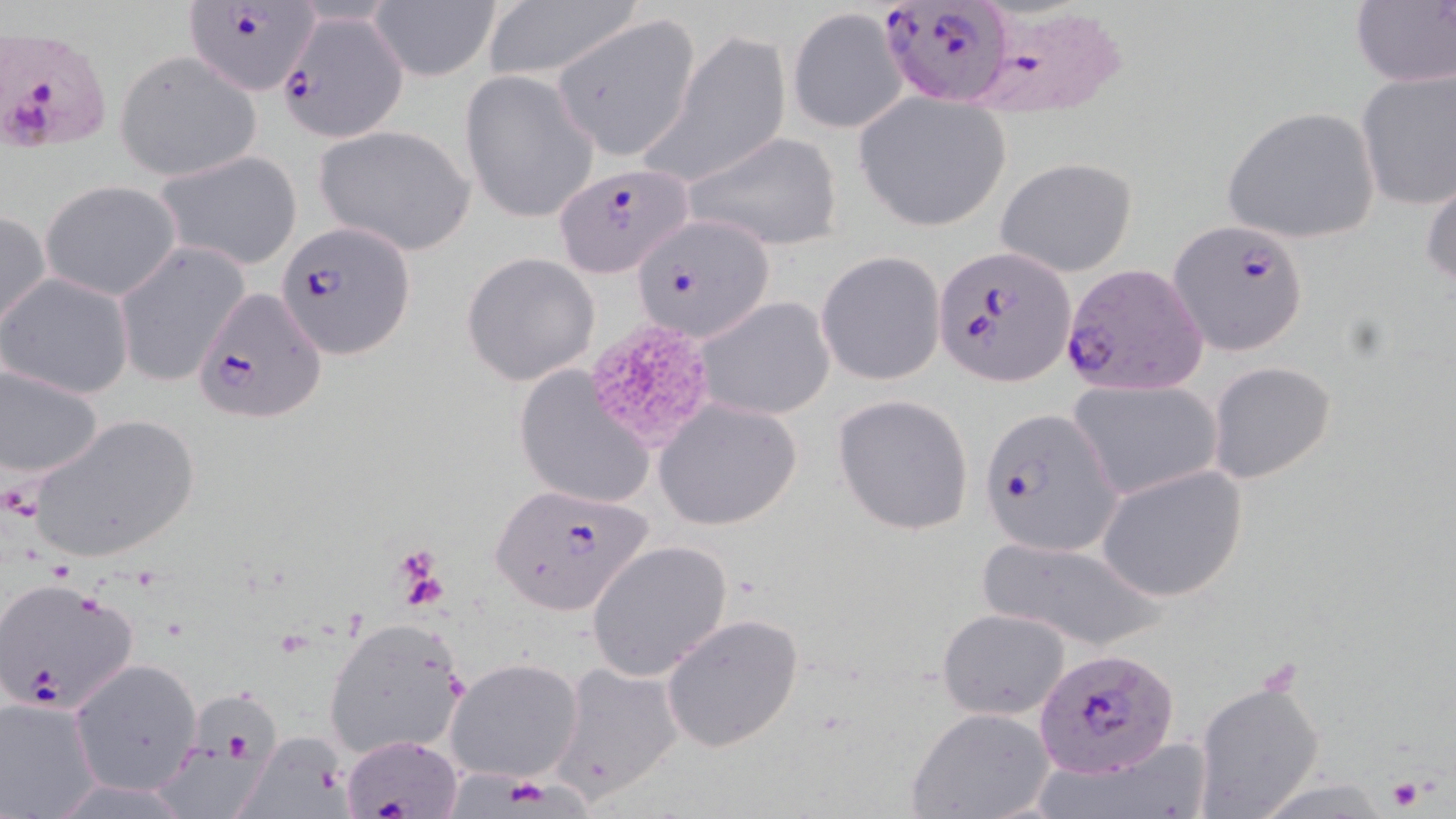

Approximate bounding boxes as (x1,y1)-(x2,y2) corner pairs in pixels. Uninfected red blood cell locations: (367,0)-(501,82), (481,1)-(640,85), (1351,2)-(1456,88), (788,7)-(905,134), (554,14)-(724,164), (641,32)-(792,188), (114,49)-(263,180), (459,68)-(601,226), (1355,69)-(1455,210), (851,95)-(1013,233), (1219,105)-(1381,244), (312,125)-(478,256), (679,130)-(842,251), (153,149)-(303,271), (995,156)-(1138,277), (1421,168)-(1456,294), (41,180)-(183,301), (0,210)-(51,335), (113,243)-(250,386), (815,251)-(946,385), (462,253)-(600,386), (0,272)-(135,400), (694,295)-(835,421), (1,361)-(106,488), (1206,361)-(1336,485), (512,365)-(656,512), (1069,379)-(1223,501), (833,394)-(974,534), (655,399)-(803,530), (29,412)-(200,565), (1097,465)-(1248,602), (587,539)-(733,682), (974,539)-(1164,650), (936,608)-(1073,718), (661,612)-(805,753), (322,615)-(468,761), (446,656)-(584,783), (69,657)-(202,796), (551,661)-(684,801), (1191,679)-(1327,819), (161,685)-(280,811), (0,696)-(106,818), (905,706)-(1055,819), (237,731)-(350,816). Platelet locations: (583,319)-(717,453), (395,547)-(447,600), (1387,776)-(1425,812). Plasmodium falciparum-infected red blood cell locations: (879,0)-(1013,107), (183,2)-(319,95), (964,3)-(1127,119), (278,10)-(409,143), (1,26)-(112,153), (554,163)-(695,278), (631,212)-(775,341), (1168,218)-(1310,356), (279,222)-(417,359), (936,247)-(1074,386), (1061,262)-(1209,396), (195,286)-(327,425), (979,406)-(1122,558), (486,480)-(657,614), (0,576)-(141,714), (1036,646)-(1179,777), (340,733)-(466,817). Slide-level diagnosis: Plasmodium falciparum. Optical microscopy. Image is 1456×819 pixels. May-Grünwald-Giemsa stain. 1000x magnification. Thin blood smear. One field of a larger specimen.